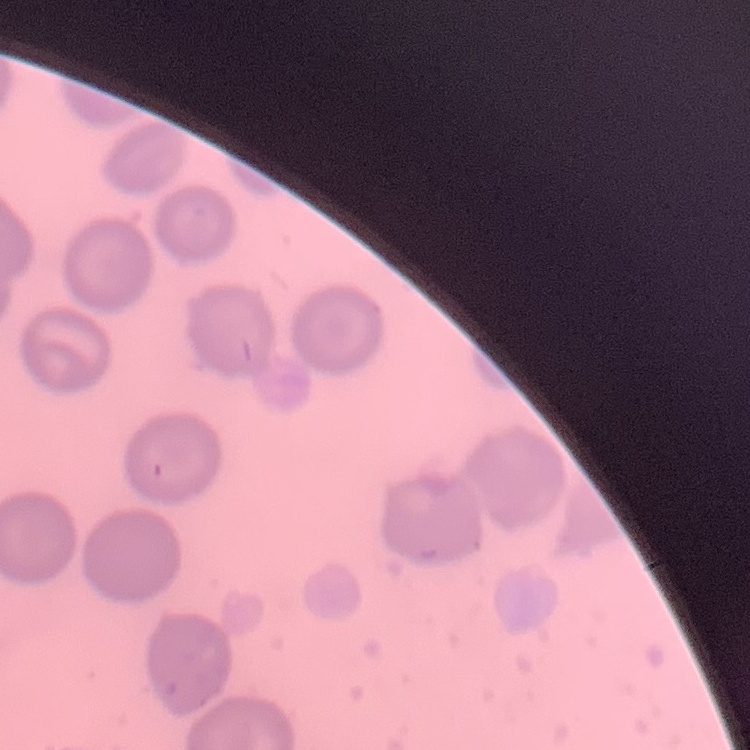
The erythrocytes show no rouleaux formation. Field's or Giemsa stain. Square crop of a larger photomicrograph. Thin peripheral smear.